State the blood parasite species.
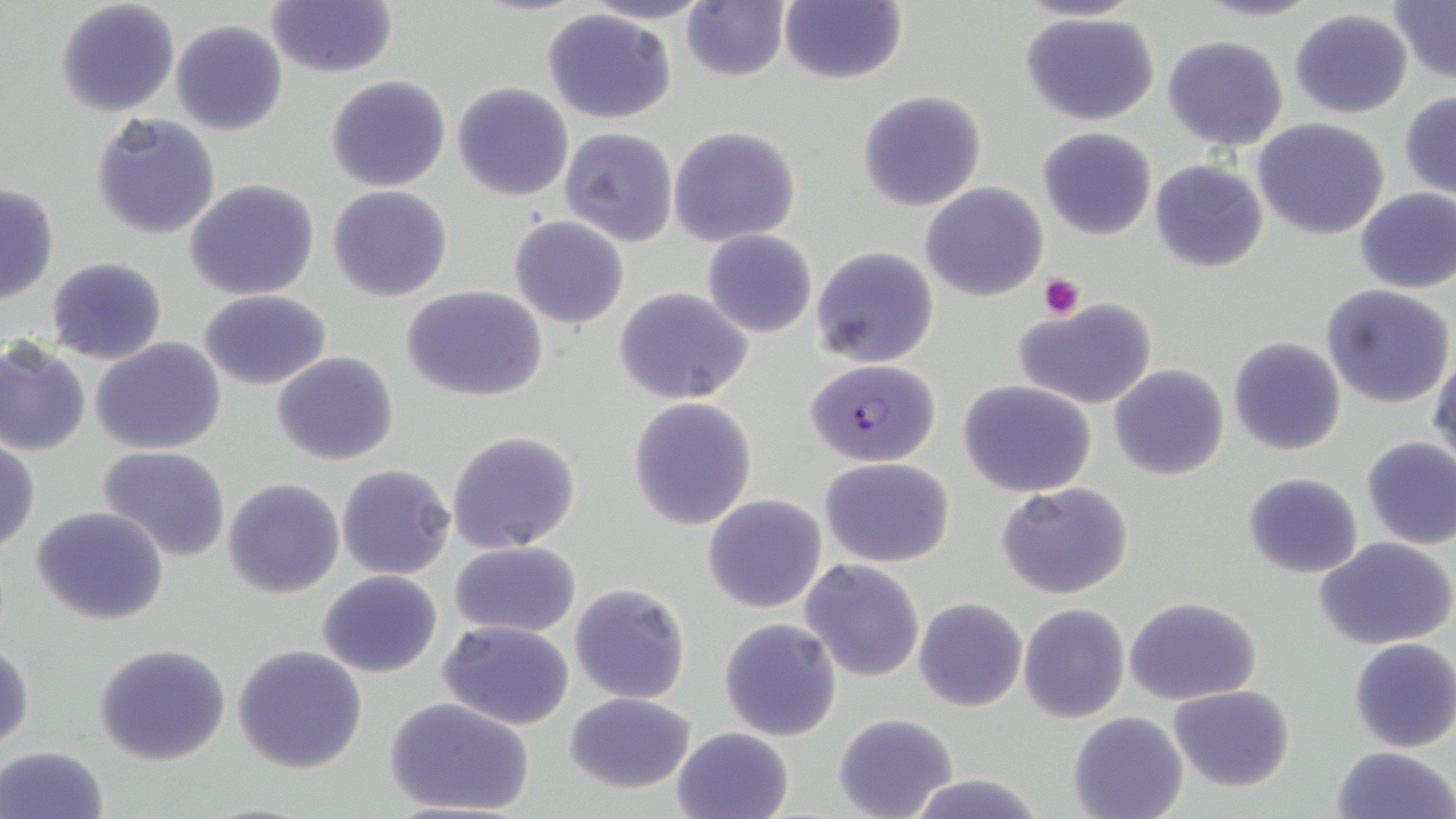

Plasmodium falciparum.

Approximate bounding boxes as named x1/y1/x2/y2 corners in pixels. Platelet locations: (x1=1039, y1=272, x2=1084, y2=319). Plasmodium falciparum-infected red blood cell locations: (x1=805, y1=359, x2=940, y2=467). Uninfected red blood cell locations: (x1=55, y1=0, x2=180, y2=117), (x1=266, y1=0, x2=396, y2=77), (x1=578, y1=0, x2=719, y2=24), (x1=780, y1=0, x2=907, y2=85), (x1=1014, y1=0, x2=1146, y2=24), (x1=1194, y1=0, x2=1325, y2=22), (x1=1386, y1=0, x2=1456, y2=85), (x1=682, y1=2, x2=790, y2=81), (x1=541, y1=9, x2=679, y2=125), (x1=1289, y1=9, x2=1414, y2=118), (x1=1018, y1=11, x2=1161, y2=126), (x1=171, y1=19, x2=287, y2=135), (x1=1163, y1=35, x2=1288, y2=151), (x1=325, y1=75, x2=451, y2=191), (x1=453, y1=82, x2=574, y2=201), (x1=857, y1=91, x2=985, y2=211), (x1=1399, y1=93, x2=1456, y2=200), (x1=90, y1=112, x2=222, y2=242), (x1=1252, y1=117, x2=1391, y2=241), (x1=668, y1=125, x2=801, y2=247), (x1=1038, y1=126, x2=1157, y2=241), (x1=560, y1=127, x2=678, y2=246), (x1=1150, y1=159, x2=1270, y2=272), (x1=185, y1=179, x2=320, y2=301), (x1=920, y1=182, x2=1049, y2=301), (x1=0, y1=183, x2=59, y2=305), (x1=328, y1=185, x2=453, y2=301), (x1=1355, y1=188, x2=1456, y2=295), (x1=509, y1=216, x2=629, y2=329), (x1=702, y1=230, x2=816, y2=339), (x1=811, y1=246, x2=939, y2=369), (x1=45, y1=258, x2=168, y2=365), (x1=403, y1=285, x2=549, y2=401), (x1=1322, y1=285, x2=1455, y2=408), (x1=613, y1=287, x2=754, y2=404), (x1=200, y1=290, x2=331, y2=389), (x1=1013, y1=298, x2=1159, y2=411), (x1=1227, y1=336, x2=1346, y2=456), (x1=0, y1=338, x2=90, y2=458), (x1=92, y1=339, x2=226, y2=455), (x1=1429, y1=347, x2=1456, y2=470), (x1=271, y1=351, x2=400, y2=465), (x1=1108, y1=364, x2=1230, y2=480), (x1=958, y1=378, x2=1097, y2=498), (x1=629, y1=396, x2=758, y2=530), (x1=446, y1=430, x2=582, y2=554), (x1=1360, y1=436, x2=1456, y2=550), (x1=1, y1=440, x2=39, y2=554), (x1=99, y1=445, x2=231, y2=561), (x1=820, y1=458, x2=953, y2=567), (x1=337, y1=464, x2=456, y2=580), (x1=1242, y1=472, x2=1364, y2=578), (x1=224, y1=478, x2=345, y2=599), (x1=996, y1=482, x2=1136, y2=601), (x1=701, y1=493, x2=828, y2=613), (x1=32, y1=505, x2=169, y2=625), (x1=1313, y1=535, x2=1456, y2=650), (x1=450, y1=541, x2=583, y2=636), (x1=799, y1=559, x2=925, y2=682), (x1=317, y1=570, x2=442, y2=678), (x1=569, y1=582, x2=691, y2=703), (x1=1124, y1=596, x2=1262, y2=705), (x1=914, y1=597, x2=1026, y2=712), (x1=1018, y1=604, x2=1129, y2=723), (x1=720, y1=618, x2=842, y2=742), (x1=438, y1=620, x2=576, y2=730), (x1=1348, y1=638, x2=1456, y2=753), (x1=1, y1=641, x2=34, y2=752), (x1=94, y1=642, x2=230, y2=765), (x1=232, y1=643, x2=368, y2=773), (x1=1167, y1=685, x2=1296, y2=791), (x1=564, y1=691, x2=695, y2=793), (x1=384, y1=697, x2=535, y2=817), (x1=833, y1=712, x2=958, y2=819), (x1=1067, y1=712, x2=1188, y2=819), (x1=670, y1=726, x2=796, y2=819), (x1=0, y1=745, x2=111, y2=819), (x1=1329, y1=745, x2=1456, y2=819), (x1=906, y1=774, x2=1043, y2=818). 1000x magnification. Single field of view. Light microscopy. Image is 1456×819 pixels. May-Grünwald-Giemsa-stained preparation. Thin blood smear.